Report the malaria status of this cell.
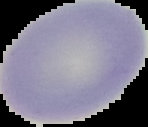

Uninfected.

Summary:
  - Image type: cell region segmented out of the field of view; surrounding area masked to black
  - Preparation: thin blood film
  - Image size: 148×127 pixels